Assess for Plasmodium parasites.
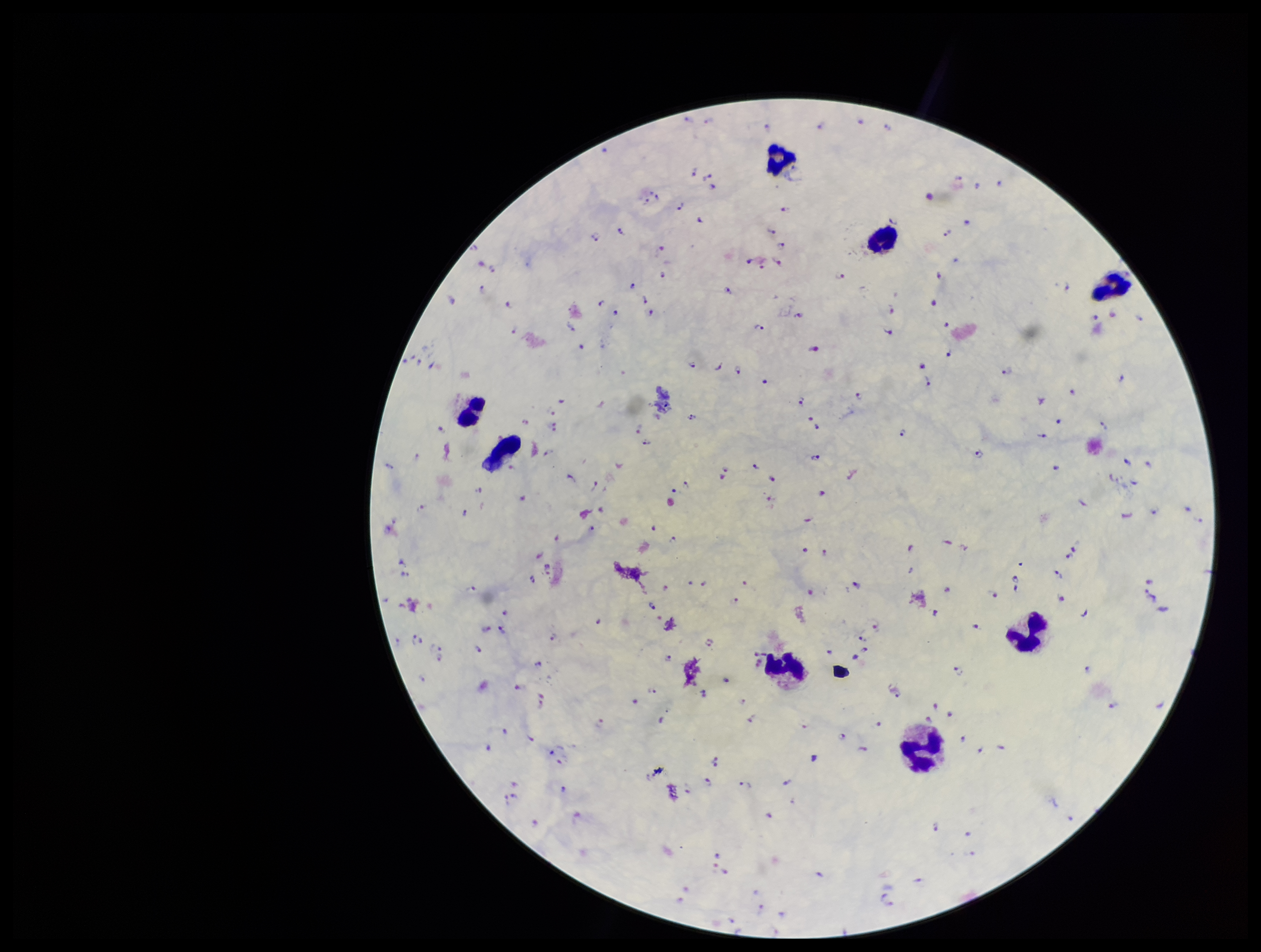

Identified.

stain = Giemsa
field of view = single
leukocyte count = 8
preparation = thick smear
parasite count = 201
capture = smartphone photograph through the microscope eyepiece
patient malaria status = infected
species reported for this patient = Plasmodium falciparum
image size = 1261×952 pixels